Mark where leukocytes are.
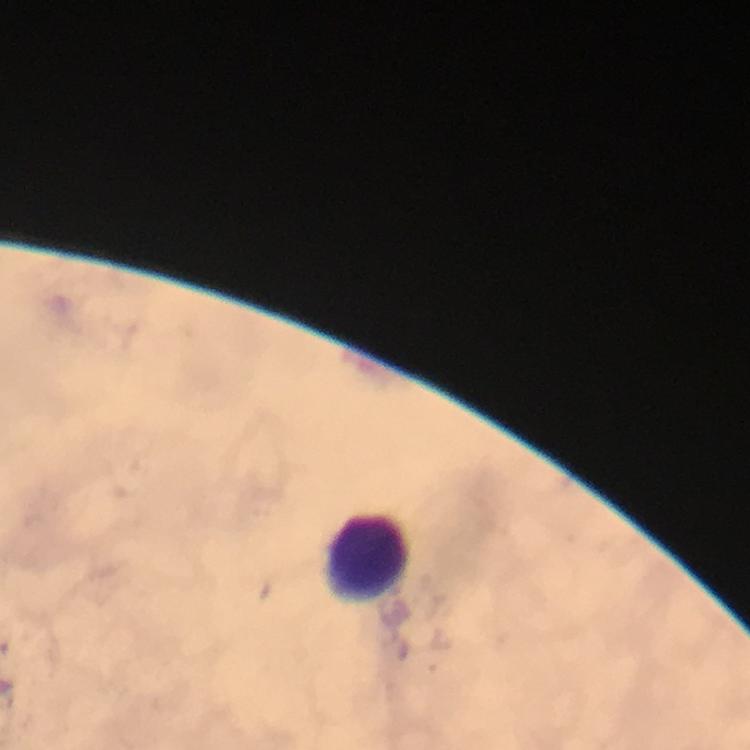

Approximate centers as (x, y) in pixels.
Leukocytes: (368, 555).

Summary:
  - Magnification: 100x
  - Stain: Giemsa
  - Capture: smartphone photograph through a microscope
  - Context: from a diagnostic examination for malaria
  - Image size: 750×750 pixels
  - Preparation: thick blood smear
  - Malaria parasites: none detected
  - Cropped from: one field of view
  - Immersion oil: applied